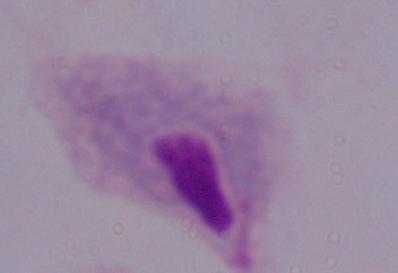
Summary:
  - Identification: trichomonad
  - Modality: micrograph
  - Magnification: 1000x